Locate every white blood cell.
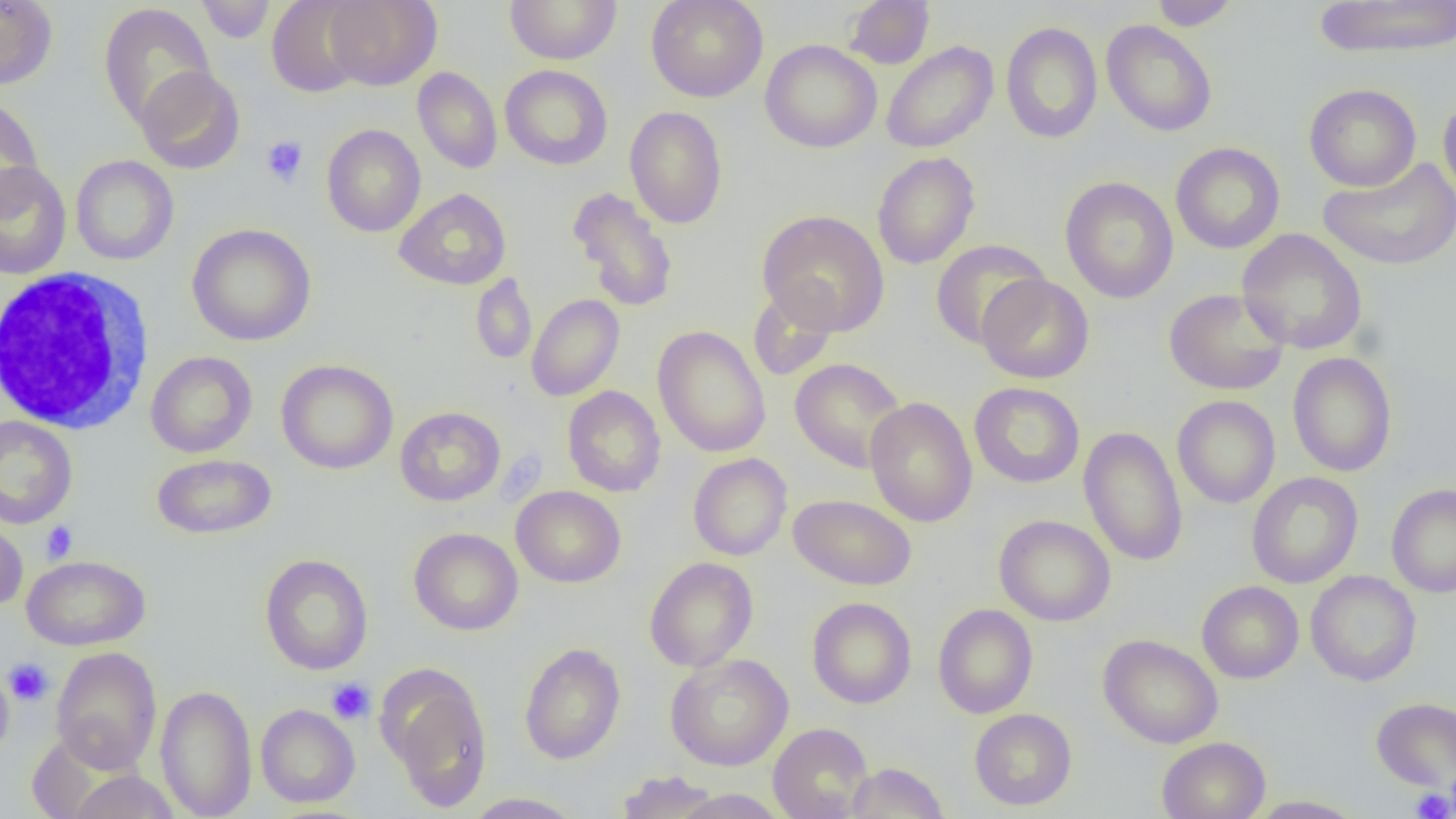
Approximate bounding boxes as (x1, y1, x2, y2) in pixels.
White blood cells: (3, 267, 153, 434).

slide-level diagnosis = negative for blood parasites
preparation = thin blood film
field of view = one of a larger specimen
uninfected red blood cell locations = approximate bounding boxes as (x1, y1, x2, y2) in pixels: (195, 0, 277, 43), (267, 0, 369, 98), (323, 0, 442, 90), (504, 0, 622, 65), (646, 0, 768, 102), (844, 0, 935, 69), (1149, 0, 1240, 30), (1313, 0, 1456, 59), (0, 1, 58, 89), (98, 3, 216, 131), (1102, 20, 1218, 137), (1001, 21, 1102, 144), (760, 39, 882, 153), (881, 41, 998, 153), (500, 65, 613, 170), (135, 66, 245, 174), (412, 67, 502, 173), (1304, 83, 1421, 191), (0, 94, 45, 212), (1438, 94, 1456, 205), (625, 105, 728, 229), (322, 124, 426, 237), (1171, 142, 1285, 254), (872, 152, 980, 269), (71, 155, 179, 265), (1318, 157, 1456, 271), (0, 161, 72, 280), (1060, 176, 1178, 303), (567, 186, 678, 312), (395, 188, 510, 290), (757, 209, 889, 335), (187, 223, 317, 346), (1237, 229, 1367, 354), (930, 240, 1050, 348), (470, 273, 537, 364), (977, 274, 1094, 383), (747, 286, 840, 382), (1164, 288, 1289, 396), (526, 294, 624, 401), (652, 325, 771, 458), (145, 351, 257, 458), (1287, 352, 1397, 477), (789, 358, 906, 473), (276, 359, 398, 475), (969, 382, 1085, 488), (562, 386, 666, 497), (1172, 395, 1281, 508), (864, 396, 978, 527), (395, 406, 505, 506), (0, 416, 77, 529), (1079, 425, 1188, 566), (688, 453, 792, 560), (151, 454, 277, 540), (1246, 472, 1363, 588), (1386, 483, 1456, 597), (511, 486, 626, 587), (788, 494, 917, 590), (994, 514, 1116, 626), (0, 515, 28, 612), (409, 527, 523, 635), (260, 553, 374, 675), (22, 555, 151, 650), (644, 557, 759, 672), (1306, 570, 1421, 686), (1197, 581, 1304, 683), (806, 597, 917, 708), (933, 604, 1038, 718), (1098, 634, 1223, 749), (519, 642, 626, 764), (51, 646, 162, 773), (665, 653, 793, 771), (379, 663, 494, 811), (0, 666, 14, 760), (155, 684, 257, 819), (1371, 697, 1456, 791), (256, 704, 360, 808), (969, 708, 1077, 811), (768, 723, 874, 819), (1157, 736, 1271, 819), (846, 761, 949, 818), (68, 770, 180, 818), (615, 771, 724, 818), (672, 789, 789, 819), (462, 792, 585, 818), (1246, 795, 1366, 818)
modality = light microscopy
magnification = 1000x
platelet locations = approximate bounding boxes as (x1, y1, x2, y2) in pixels: (261, 136, 308, 187), (41, 521, 78, 564), (3, 658, 54, 706), (326, 678, 375, 725), (1411, 787, 1454, 818)
image size = 1456×819 pixels